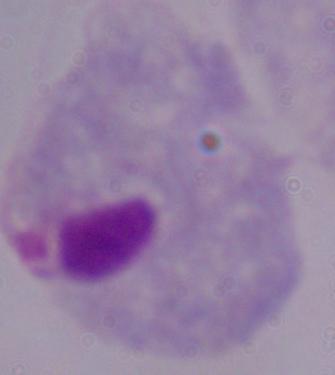
Micrograph. A trichomonad is shown. 1000x magnification.